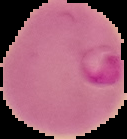

preparation: thin blood film
image_type: cell region segmented out of the field of view; surrounding area masked to black
malaria_status: parasitized
image_size: 127×139 pixels